Assess this cell for malaria.
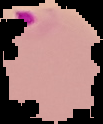
Parasitized.

image type = segmented cell region on a black background
image size = 103×124 pixels
preparation = thin blood film